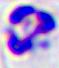

400x magnification. A leukocyte is shown. Photomicrograph.